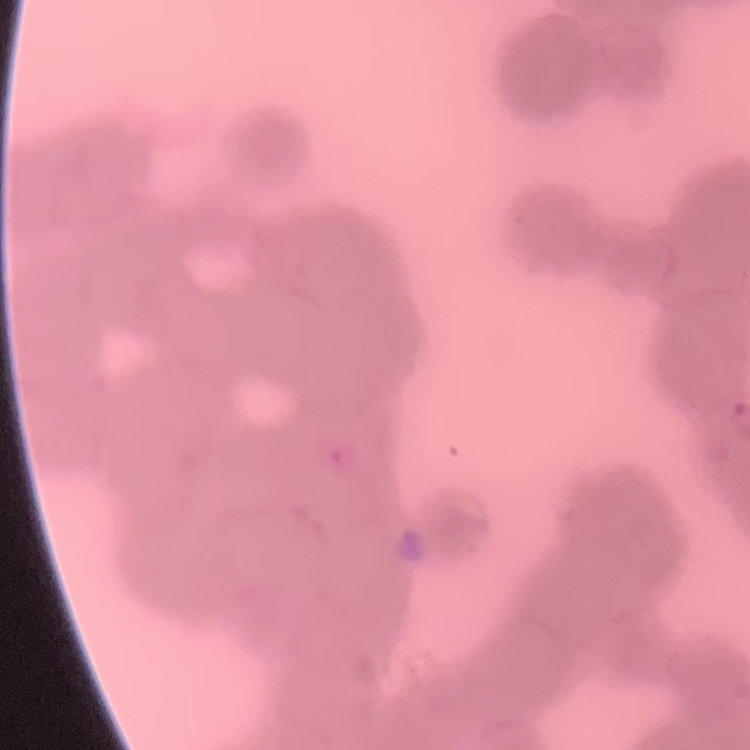
red_blood_cell_morphology: rouleaux formation
image_type: square crop of a larger photomicrograph
preparation: thin peripheral smear
stain: Field's or Giemsa